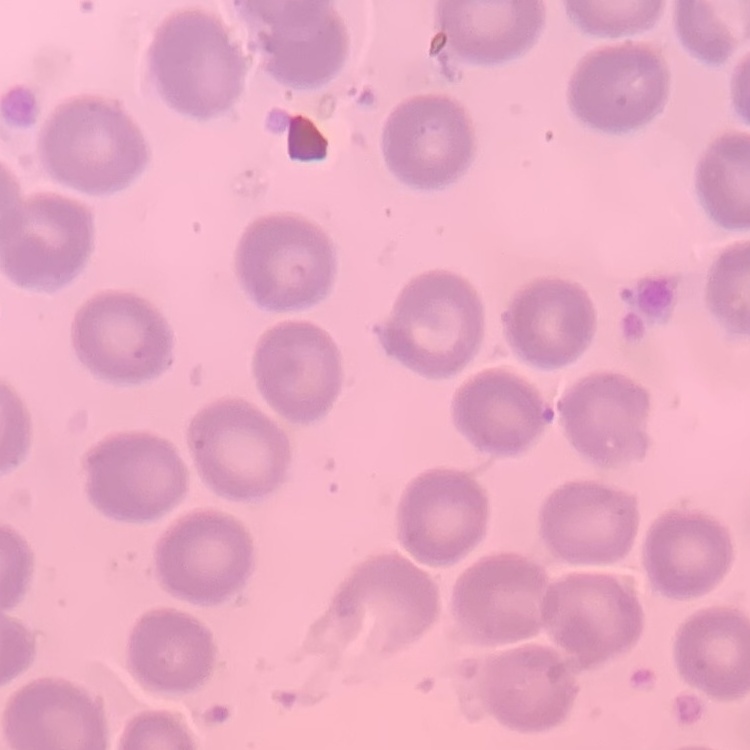 The red blood cells show no rouleaux formation. Thin blood film. One tile cut from a larger photomicrograph. Field's or Giemsa stain.